Mark where platelets are.
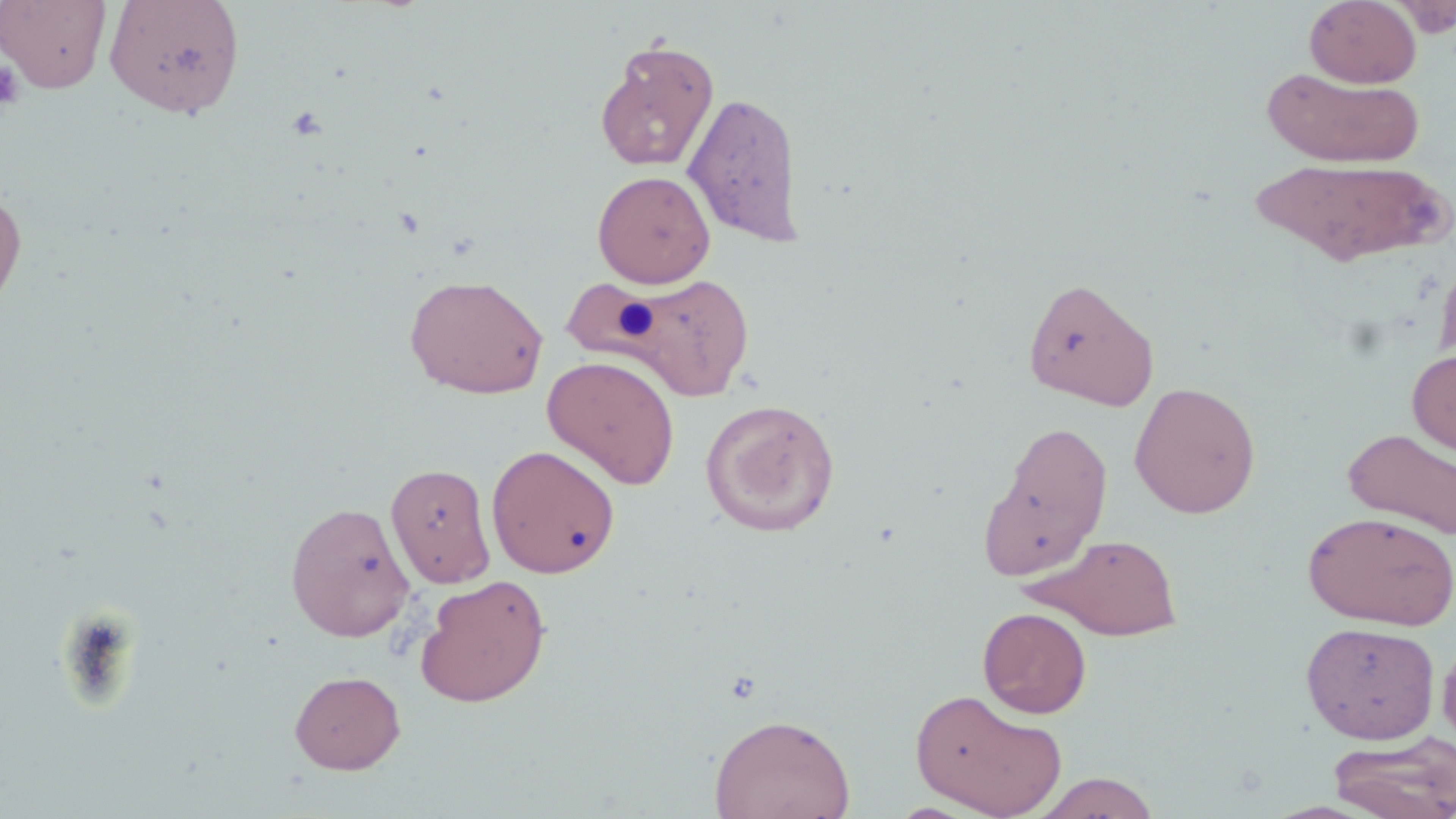

Approximate bounding boxes as [x1, y1, x2, y2] in pixels.
Platelets: [0, 61, 24, 110].

Uninfected red blood cell locations: [0, 0, 112, 94], [105, 0, 246, 120], [1304, 0, 1421, 87], [1390, 0, 1453, 37], [594, 38, 719, 172], [1263, 66, 1424, 168], [683, 90, 805, 247], [1249, 156, 1450, 267], [592, 170, 717, 287], [0, 184, 27, 317], [1435, 250, 1456, 369], [557, 271, 757, 401], [405, 274, 548, 400], [1022, 276, 1159, 410], [1407, 347, 1456, 457], [542, 354, 681, 490], [1128, 381, 1262, 519], [700, 397, 841, 537], [979, 419, 1113, 579], [1342, 427, 1456, 540], [487, 444, 620, 579], [385, 462, 496, 588], [284, 500, 415, 642], [1302, 510, 1455, 630], [1028, 532, 1184, 641], [415, 574, 551, 708], [977, 606, 1092, 719], [1301, 622, 1439, 744], [1437, 632, 1456, 756], [289, 669, 406, 774], [909, 688, 1068, 818], [708, 713, 856, 819], [1328, 732, 1456, 819], [1032, 771, 1160, 818]. Slide-level diagnosis: negative for blood parasites. Image is 1456×819 pixels. One field of a larger specimen. Thin blood film. Captured at 1000x magnification. Optical microscopy. May-Grünwald-Giemsa stain.